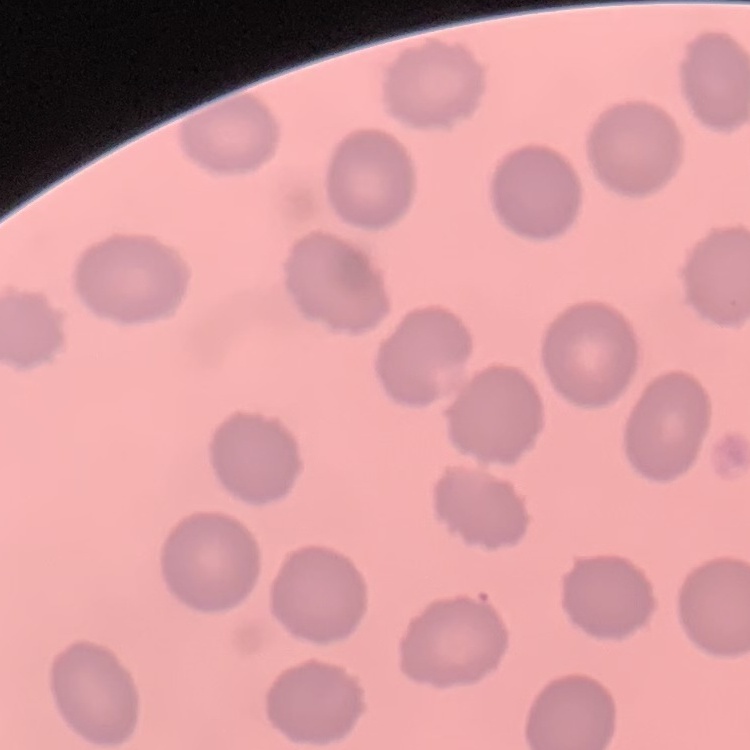
{
  "erythrocyte_morphology": "no rouleaux formation",
  "image_type": "square crop of a larger photomicrograph",
  "preparation": "thin blood film",
  "stain": "Field's or Giemsa"
}